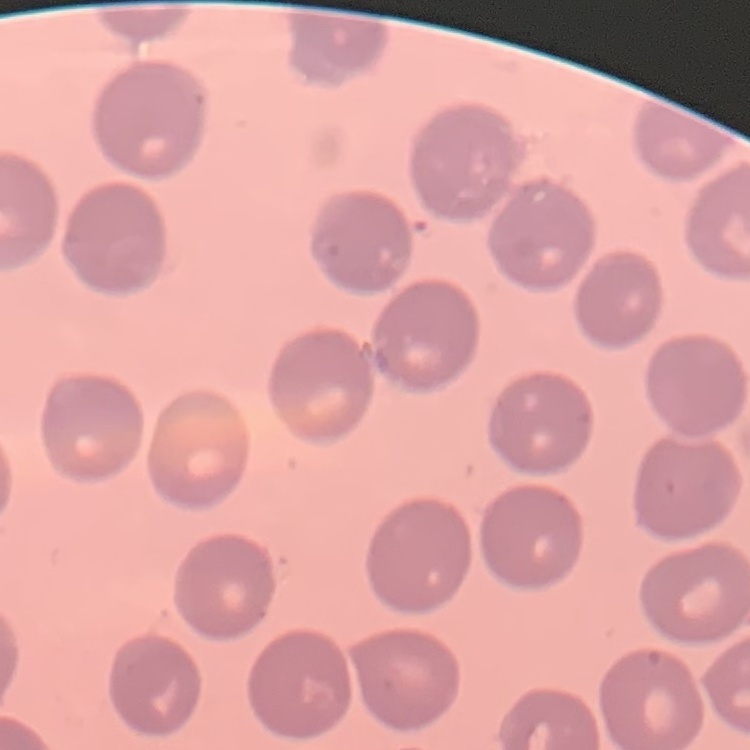
erythrocyte_morphology: no rouleaux formation
preparation: thin blood smear
stain: Field's or Giemsa
image_type: square crop of a larger photomicrograph